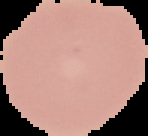
Summary:
  - Result: negative for Plasmodium parasites
  - Image type: segmented cell region with the area outside set to black
  - Preparation: thin blood smear
  - Image size: 148×136 pixels